Describe the morphology of the red blood cells.
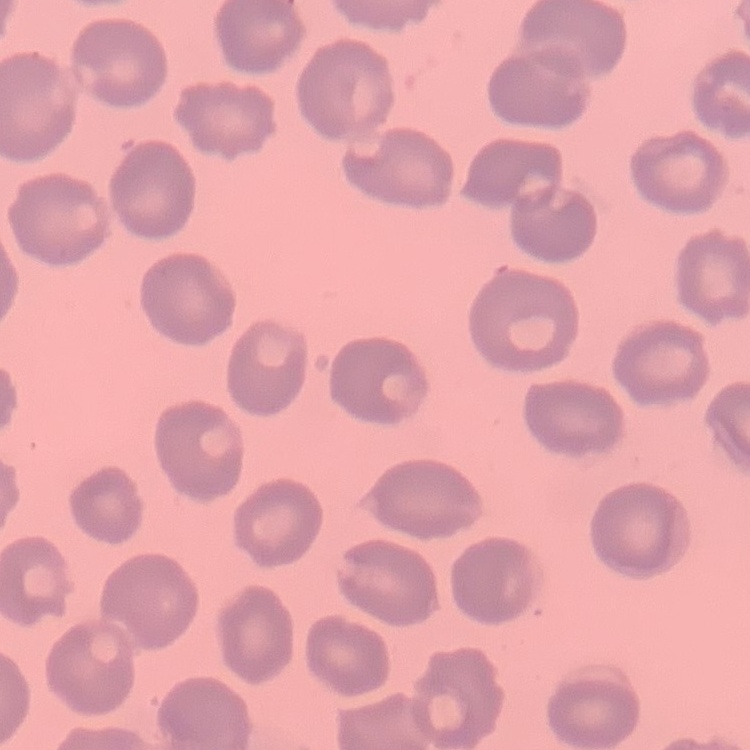
They show no rouleaux formation.

{
  "preparation": "thin blood film",
  "stain": "Field's or Giemsa",
  "image_type": "square crop of a larger photomicrograph"
}